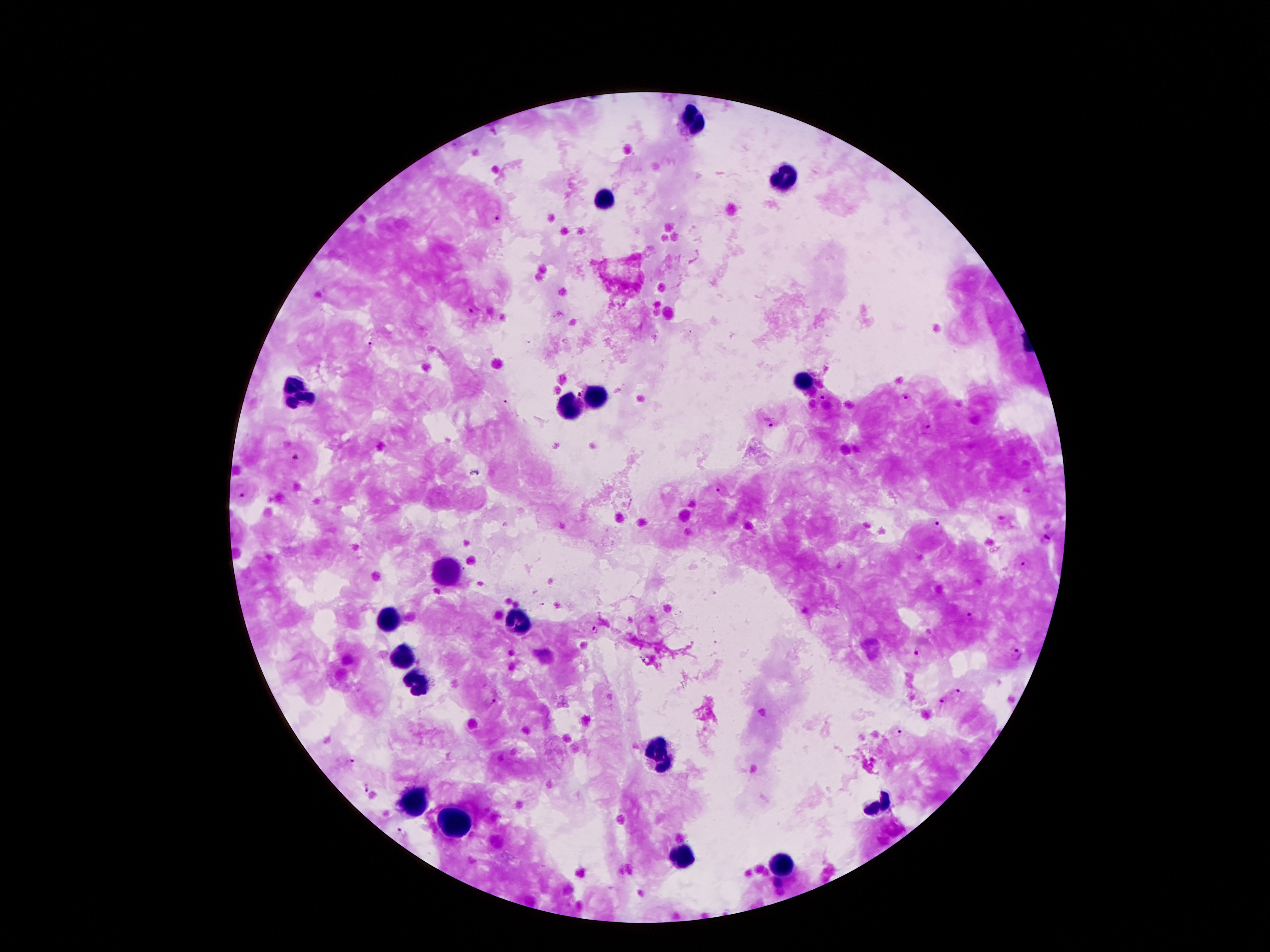
Approximate centers as [x, y] in pixels. Malaria parasite locations: [498, 220], [469, 311], [372, 345], [578, 395], [905, 396], [821, 398], [504, 403], [768, 422], [928, 429], [298, 456], [721, 489], [241, 493], [939, 527], [1045, 539], [1026, 564], [969, 615], [594, 632], [917, 653], [1016, 655], [959, 693], [491, 700], [941, 702], [896, 733], [351, 762], [366, 786], [404, 833], [777, 884]. Leukocyte locations: [695, 124], [781, 178], [603, 195], [803, 385], [294, 393], [593, 398], [568, 408], [450, 568], [393, 620], [517, 623], [403, 655], [413, 682], [657, 751], [418, 800], [880, 800], [457, 825], [682, 857], [784, 865]. Thick blood smear. Image is 1270×952 pixels. Giemsa stain. One field from this slide. Smartphone photograph taken through the microscope eyepiece. Patient malaria status: infected with Plasmodium falciparum. 100x magnification.